Locate Plasmodium parasites and leukocytes.
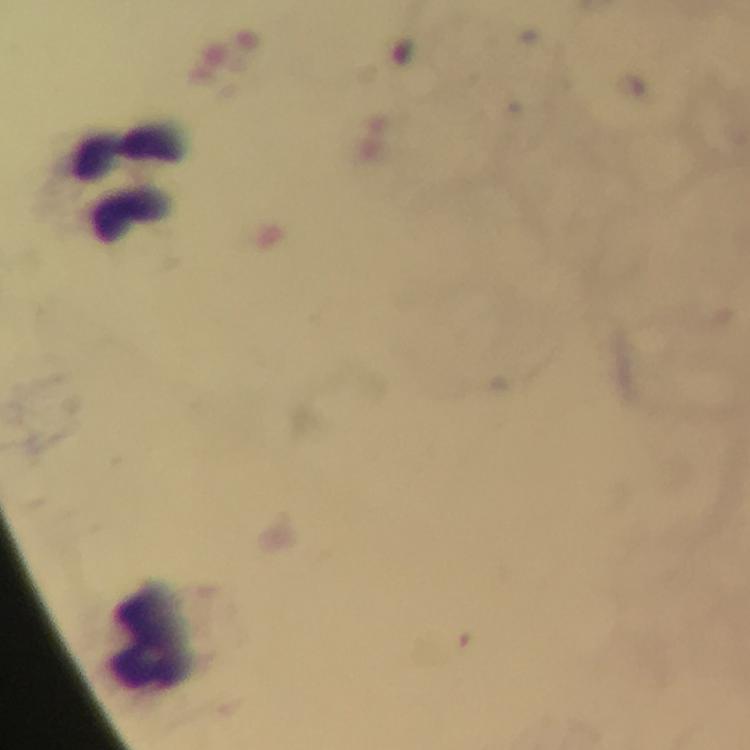

No Plasmodium parasites detected.
Approximate centers as [x, y] in pixels.
Leukocytes: [121, 180], [142, 635].

Giemsa stain. Thick smear. Photographed with a smartphone mounted on the microscope. Immersion oil was used. Image is 750×750 pixels. From a diagnostic examination for malaria. Cropped region of a single field of view. At 100x magnification.